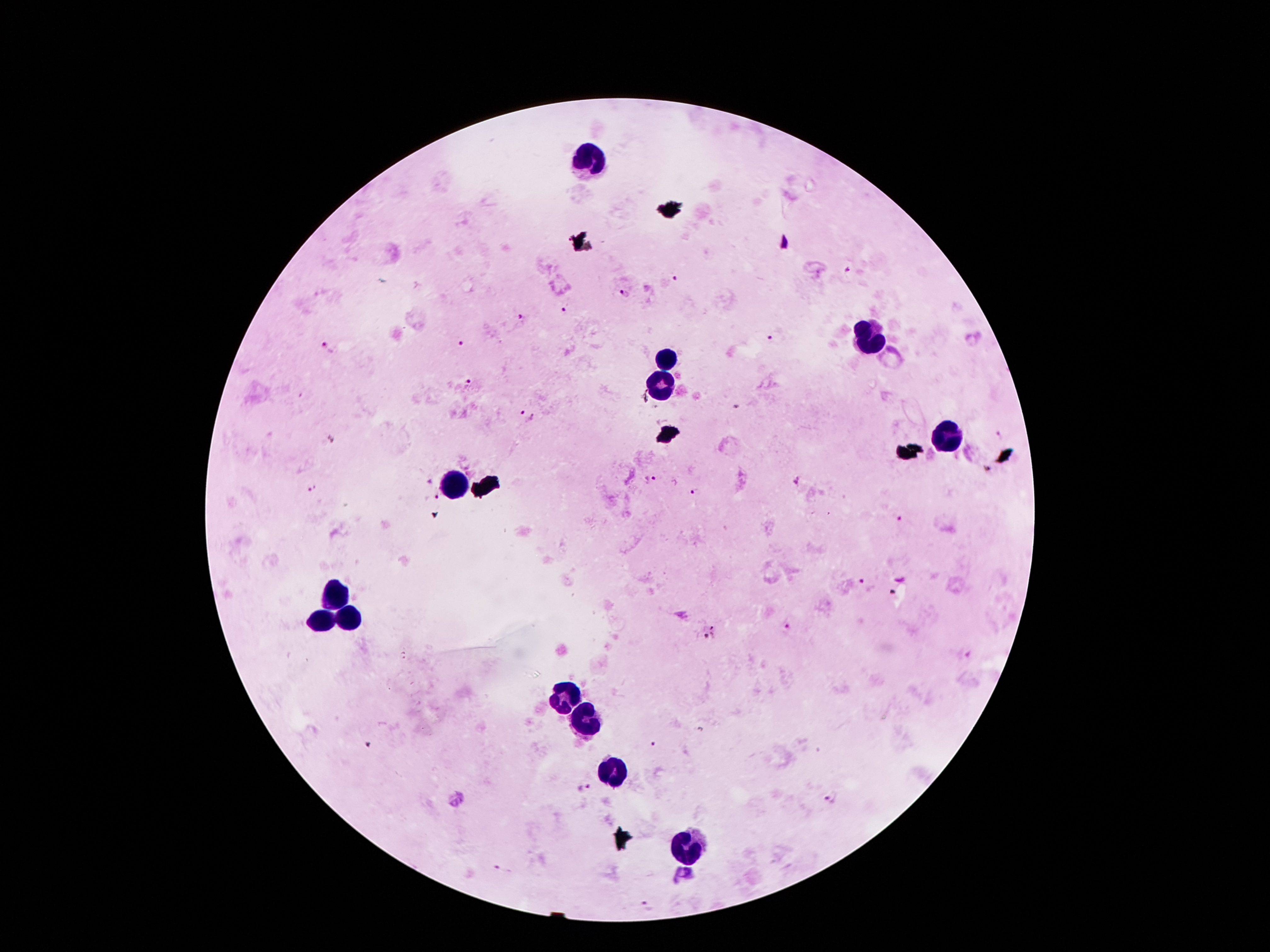

stain: Giemsa
field_of_view: one from this slide
leukocyte_locations: 'approximate centers as {x, y} in pixels: {595, 160}, {866, 338}, {671, 361}, {662, 385}, {944, 434}, {456, 485}, {337, 595}, {345, 618}, {318, 620}, {563, 698}, {584, 720}, {616, 774}, {685, 846}'
magnification: 100x
plasmodium_parasite_locations: 'approximate centers as {x, y} in pixels: {849, 271}, {673, 279}, {625, 293}, {565, 309}, {521, 316}, {770, 338}, {462, 343}, {327, 348}, {470, 382}, {736, 408}, {526, 415}, {999, 434}, {649, 479}, {798, 481}, {426, 482}, {313, 489}, {693, 491}, {437, 498}, {900, 518}, {862, 581}, {787, 629}, {709, 635}, {584, 790}, {828, 801}'
capture: smartphone through the microscope eyepiece
image_size: 1270×952 pixels
patient_malaria_status: infected with Plasmodium falciparum
preparation: thick peripheral-blood smear